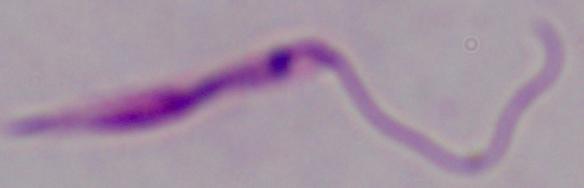

Summary:
  - Identification: Leishmania
  - Modality: photomicrograph
  - Magnification: 1000x